Outline every malaria parasite.
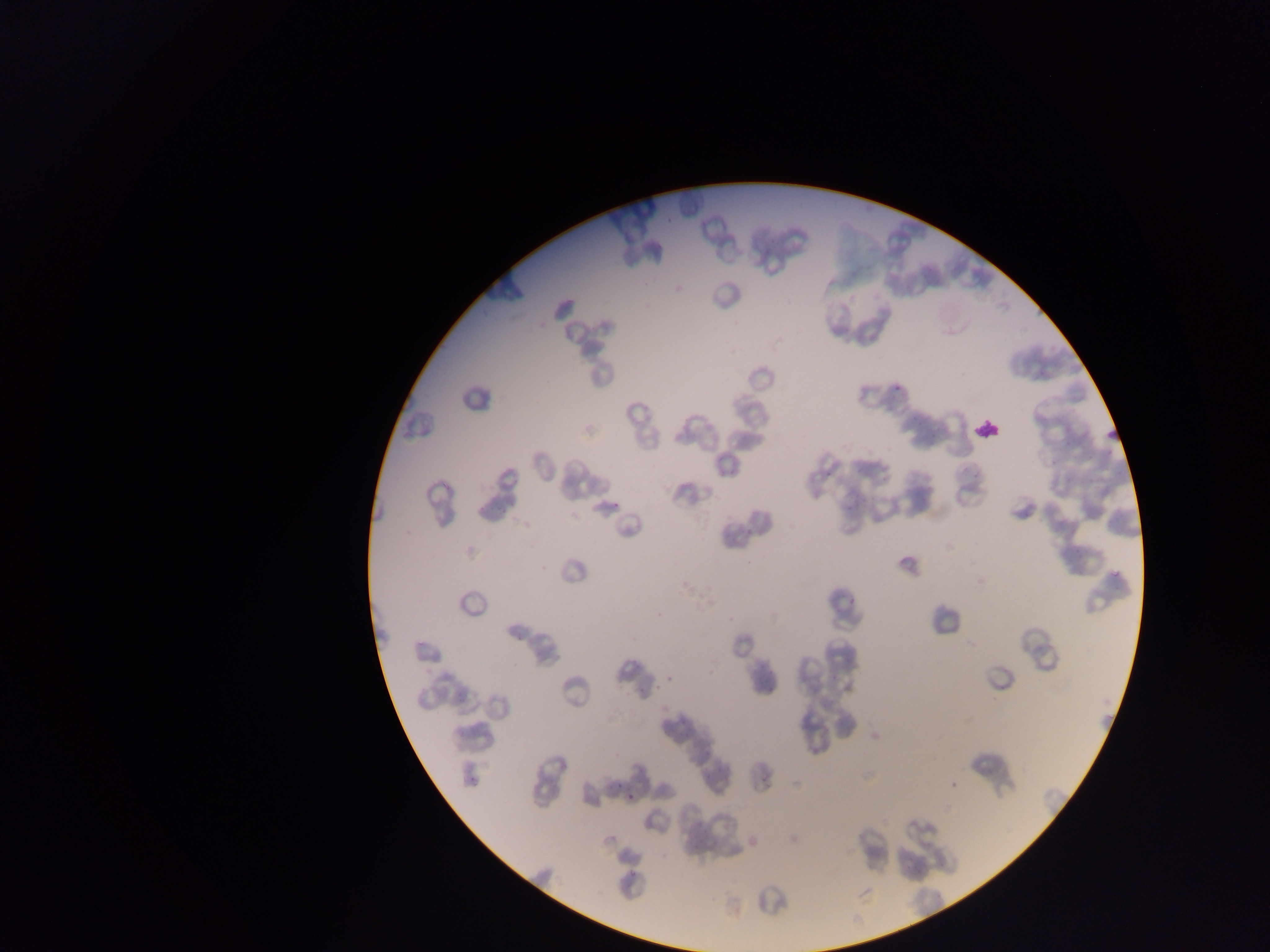
Approximate bounding boxes as [left, top, right, bottom] in pixels.
Malaria parasites: [891, 383, 905, 392], [611, 500, 622, 509], [847, 597, 861, 608], [667, 673, 681, 684], [466, 773, 476, 787], [626, 789, 641, 805], [629, 870, 639, 876].

image size = 1270×952 pixels
leukocyte locations = approximate bounding boxes as [left, top, right, bottom] in pixels: [970, 414, 1006, 448]
country = Ghana
preparation = thin blood film
field of view = single
capture = mobile-phone photograph through a microscope